Outline each blood parasite and name the species.
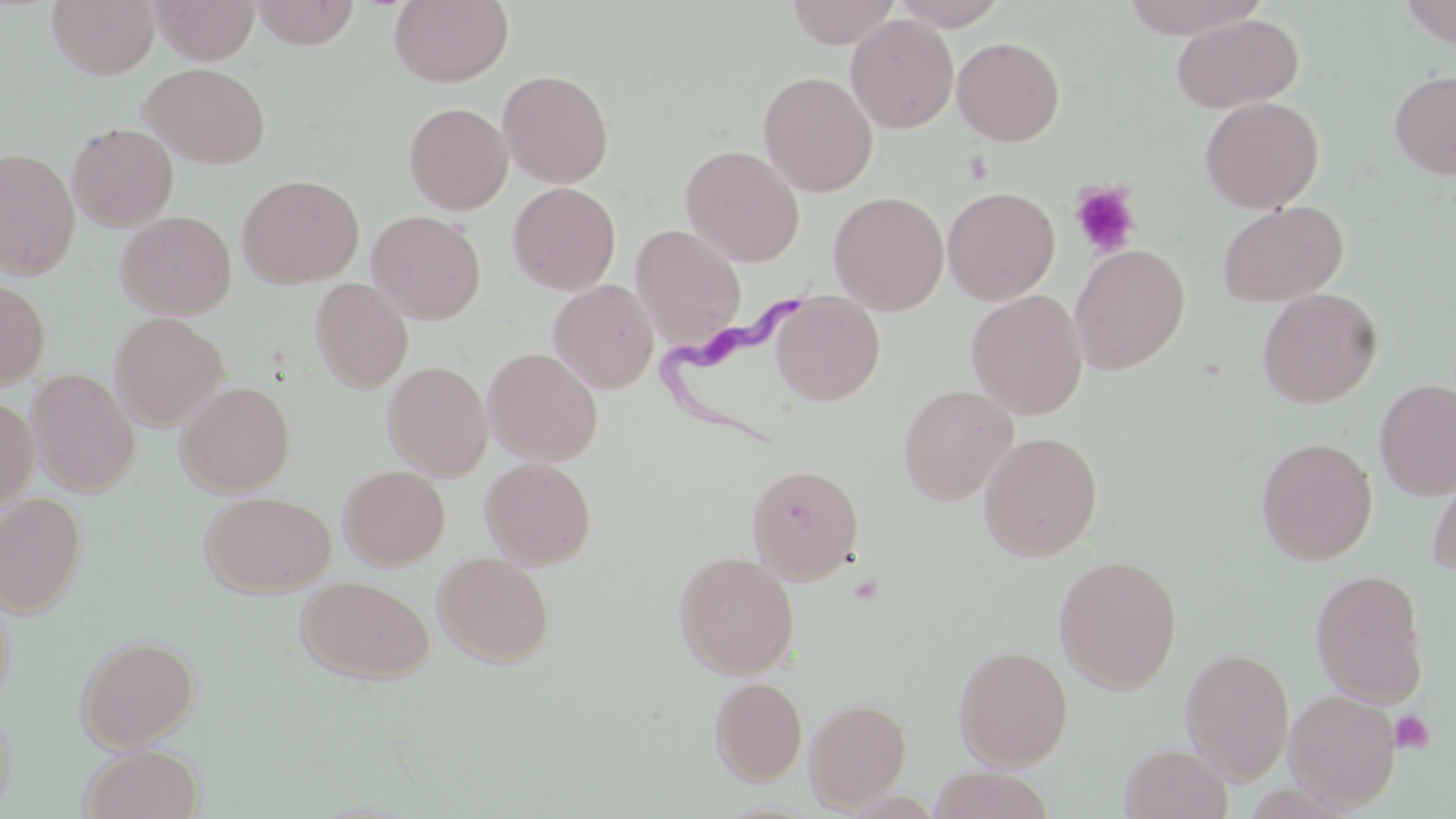

Approximate bounding boxes as (x1, y1, x2, y2) in pixels.
Trypanosoma brucei: (654, 279, 819, 447).
No Plasmodium falciparum, Plasmodium ovale, Plasmodium malariae, Plasmodium vivax, or Babesia divergens observed.

slide_level_diagnosis: Trypanosoma brucei
stain: May-Grünwald-Giemsa
magnification: 1000x
image_size: 1456×819 pixels
platelet_locations: 'approximate bounding boxes as (x1, y1, x2, y2) in pixels: (1069, 182, 1141, 259), (1390, 710, 1435, 753)'
field_of_view: one of a larger specimen
uninfected_red_blood_cell_locations: 'approximate bounding boxes as (x1, y1, x2, y2) in pixels: (48, 0, 160, 79), (250, 0, 361, 48), (388, 0, 513, 87), (784, 0, 900, 47), (889, 0, 1010, 29), (1119, 0, 1269, 37), (1398, 0, 1456, 48), (152, 1, 260, 64), (1171, 13, 1304, 113), (845, 14, 958, 133), (952, 36, 1065, 146), (140, 62, 271, 168), (498, 69, 614, 188), (1390, 69, 1456, 180), (758, 71, 879, 197), (1199, 96, 1324, 213), (403, 102, 512, 214), (67, 123, 179, 231), (680, 144, 805, 267), (0, 148, 79, 280), (238, 174, 364, 288), (507, 182, 621, 294), (942, 187, 1060, 304), (828, 191, 948, 314), (1216, 201, 1349, 307), (367, 210, 486, 324), (115, 211, 237, 319), (630, 224, 746, 347), (1070, 243, 1190, 374), (0, 277, 50, 388), (310, 278, 413, 394), (549, 279, 659, 394), (1257, 288, 1382, 408), (966, 289, 1088, 419), (770, 292, 885, 406), (109, 312, 229, 430), (482, 347, 603, 466), (382, 360, 492, 480), (26, 368, 140, 495), (1374, 379, 1456, 500), (176, 380, 296, 496), (898, 384, 1018, 505), (0, 394, 39, 510), (978, 431, 1103, 561), (1256, 437, 1377, 564), (1426, 454, 1456, 576), (480, 457, 596, 568), (746, 463, 864, 583), (338, 465, 450, 570), (201, 491, 336, 596), (0, 492, 86, 616), (434, 551, 555, 667), (674, 551, 800, 678), (1053, 554, 1183, 693), (1311, 568, 1429, 708), (296, 575, 434, 685), (76, 635, 200, 752), (954, 644, 1073, 770), (1180, 646, 1295, 784), (709, 676, 808, 786), (1284, 689, 1402, 809), (805, 696, 912, 812), (0, 699, 14, 816), (1119, 743, 1232, 819), (79, 744, 204, 819), (928, 767, 1058, 819)'
modality: light microscopy
preparation: thin blood smear